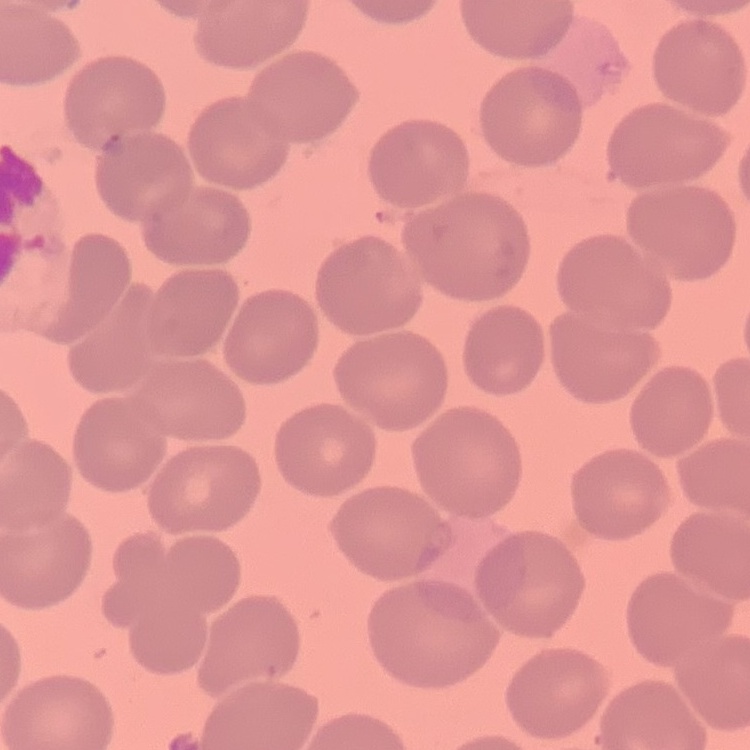
{
  "erythrocyte_morphology": "no rouleaux formation",
  "image_type": "one tile cut from a larger photomicrograph",
  "stain": "Field's or Giemsa",
  "preparation": "thin blood smear"
}